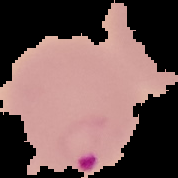

From a thin blood smear. Cell region segmented out of the field of view; the surrounding area is masked to black. Image is 178×178 pixels. Result: malaria parasites detected.